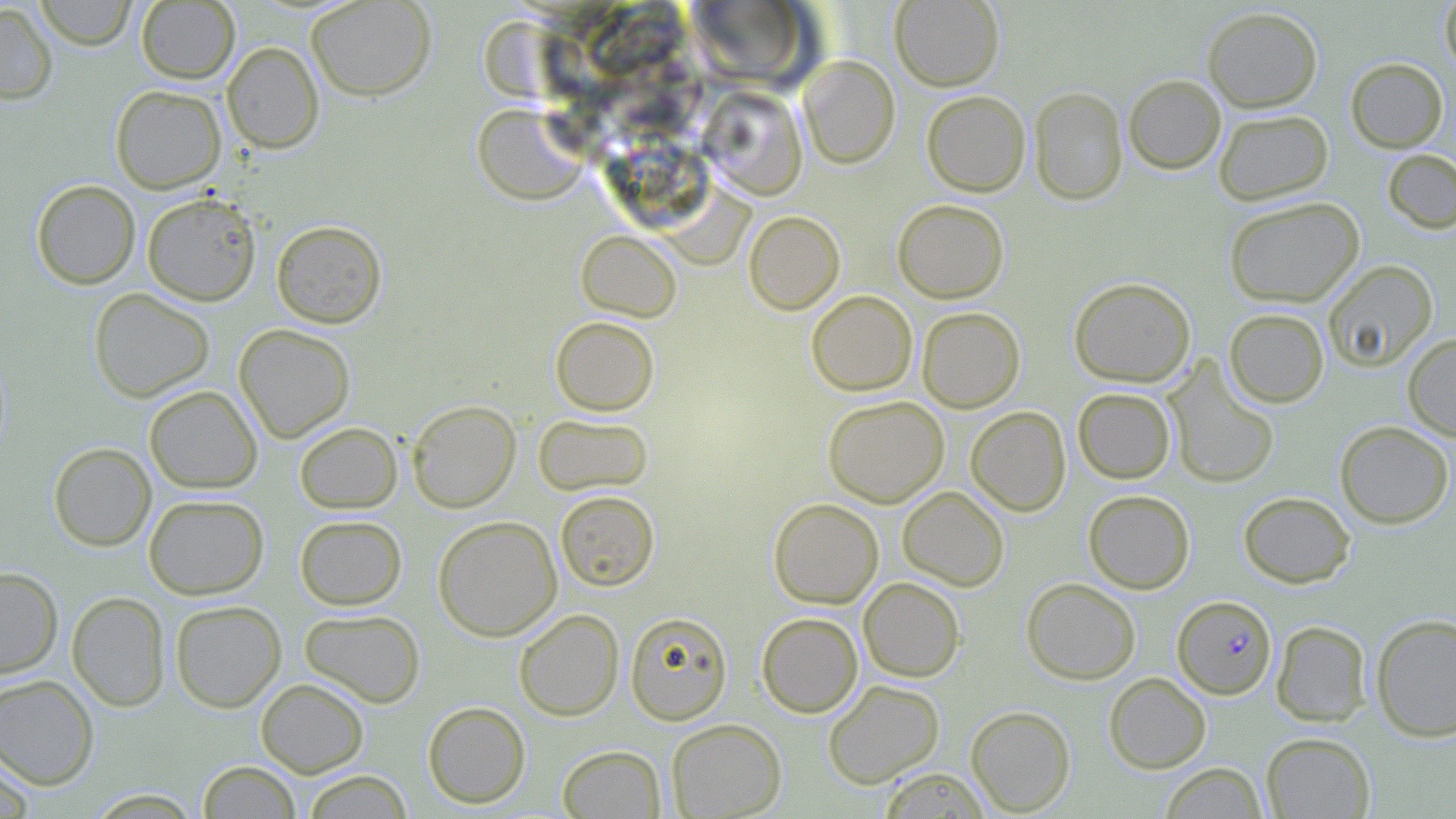
Summary:
  - Coordinate format: approximate bounding boxes as [x1, y1, x2, y2] in pixels
  - Plasmodium falciparum-infected red blood cell locations: [1172, 595, 1277, 699]
  - Uninfected red blood cell locations: [34, 0, 137, 50], [306, 0, 437, 101], [891, 0, 1005, 91], [1439, 0, 1456, 75], [136, 1, 240, 85], [685, 1, 819, 89], [0, 3, 58, 104], [1202, 6, 1323, 112], [222, 41, 324, 154], [798, 55, 899, 168], [1345, 57, 1449, 152], [1123, 74, 1226, 174], [110, 85, 226, 193], [700, 86, 808, 199], [1029, 86, 1128, 205], [921, 90, 1031, 196], [472, 103, 590, 205], [1213, 109, 1334, 205], [1383, 149, 1456, 234], [31, 179, 141, 289], [661, 185, 755, 270], [142, 192, 261, 306], [1224, 196, 1364, 308], [893, 199, 1009, 303], [744, 210, 845, 314], [271, 219, 387, 328], [576, 230, 682, 322], [1322, 259, 1438, 372], [1069, 276, 1196, 388], [88, 287, 215, 402], [806, 290, 917, 396], [917, 306, 1025, 412], [1224, 308, 1329, 407], [550, 316, 660, 416], [234, 323, 356, 442], [1402, 332, 1456, 441], [1163, 358, 1280, 490], [144, 385, 263, 494], [1073, 387, 1176, 484], [823, 395, 949, 508], [407, 400, 521, 512], [966, 406, 1071, 516], [533, 413, 654, 496], [295, 421, 402, 514], [1334, 421, 1454, 528], [48, 442, 156, 551], [897, 486, 1009, 591], [554, 490, 660, 591], [1083, 490, 1195, 594], [1238, 491, 1356, 588], [143, 494, 269, 599], [769, 498, 884, 608], [294, 514, 407, 610], [433, 515, 562, 641], [0, 567, 63, 679], [858, 577, 965, 682], [1021, 577, 1141, 684], [67, 591, 170, 711], [169, 600, 286, 712], [299, 608, 426, 708], [513, 609, 624, 721], [625, 611, 733, 724], [756, 613, 864, 717], [1370, 614, 1456, 742], [1271, 620, 1372, 726], [1103, 672, 1211, 774], [0, 674, 99, 790], [256, 678, 369, 777], [823, 679, 945, 788], [422, 701, 531, 809], [965, 705, 1076, 816], [666, 718, 787, 818], [1261, 732, 1376, 818], [557, 745, 665, 818], [0, 751, 36, 819], [197, 760, 301, 818], [1159, 762, 1267, 818], [878, 768, 990, 818], [300, 770, 413, 818]
  - Slide-level diagnosis: Plasmodium falciparum
  - Stain: May-Grünwald-Giemsa
  - Field of view: one of a larger specimen
  - Modality: light microscopy
  - Image size: 1456×819 pixels
  - Preparation: thin blood smear
  - Magnification: 1000x